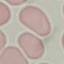

Summary:
  - Result: negative for malaria parasites
  - Image type: automatically extracted cell patch, resized to 64 × 64 pixels
  - Stain: Giemsa
  - Preparation: thin blood film
  - Capture: smartphone through the microscope eyepiece